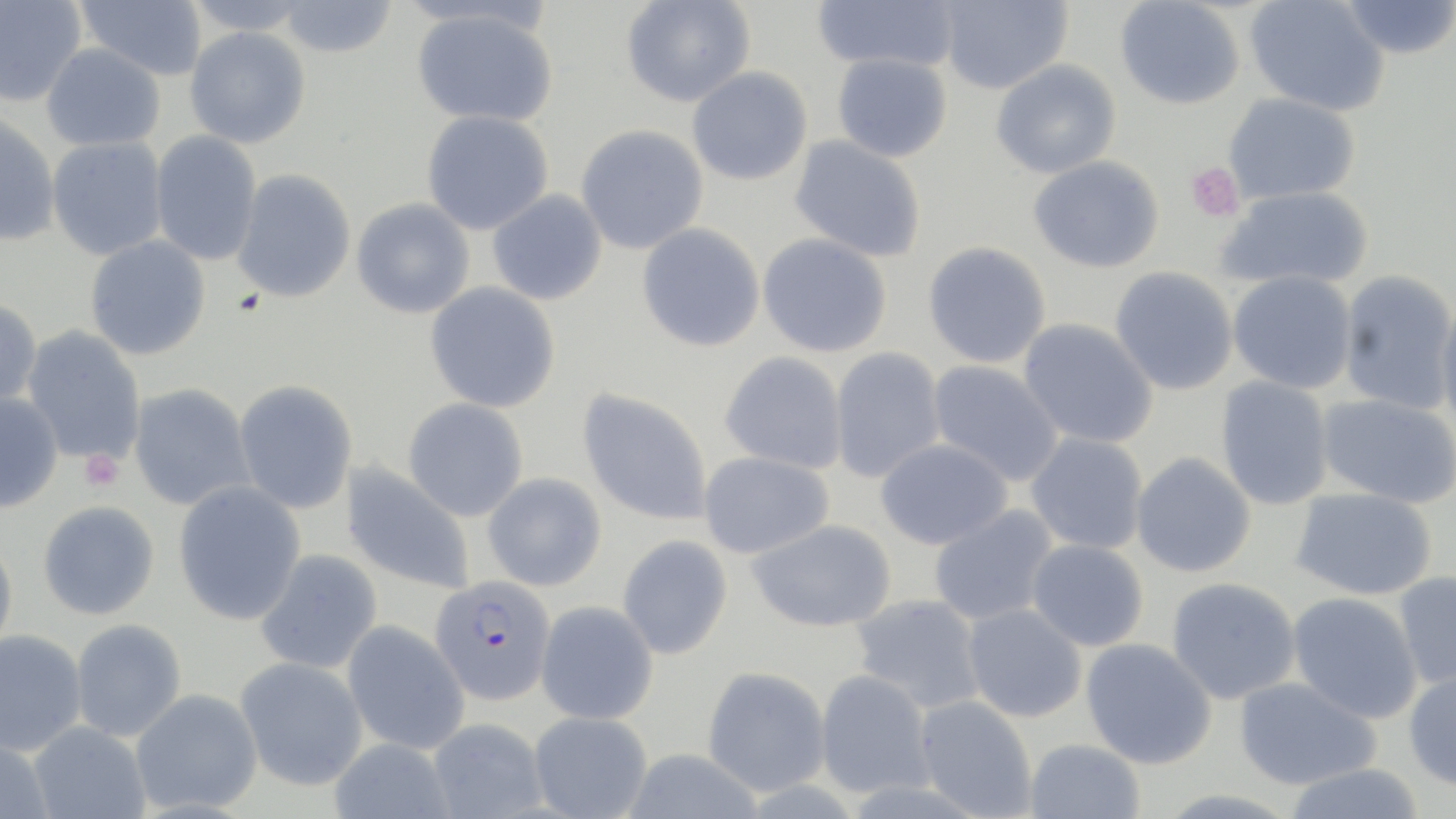 Approximate bounding boxes as named x1/y1/x2/y2 corners in pixels. Plasmodium falciparum-infected red blood cell locations: (x1=430, y1=575, x2=556, y2=705). Platelet locations: (x1=1184, y1=162, x2=1244, y2=222), (x1=79, y1=450, x2=125, y2=493). Uninfected red blood cell locations: (x1=75, y1=0, x2=208, y2=81), (x1=182, y1=0, x2=316, y2=36), (x1=276, y1=0, x2=398, y2=58), (x1=620, y1=0, x2=756, y2=108), (x1=810, y1=0, x2=960, y2=72), (x1=936, y1=0, x2=1072, y2=94), (x1=1245, y1=0, x2=1390, y2=116), (x1=1336, y1=0, x2=1456, y2=61), (x1=0, y1=1, x2=87, y2=107), (x1=1115, y1=1, x2=1245, y2=110), (x1=410, y1=7, x2=558, y2=128), (x1=184, y1=27, x2=311, y2=148), (x1=41, y1=42, x2=166, y2=152), (x1=832, y1=53, x2=952, y2=163), (x1=991, y1=59, x2=1122, y2=179), (x1=687, y1=67, x2=813, y2=186), (x1=1223, y1=93, x2=1361, y2=204), (x1=421, y1=110, x2=554, y2=235), (x1=0, y1=112, x2=61, y2=247), (x1=576, y1=125, x2=709, y2=255), (x1=149, y1=130, x2=262, y2=266), (x1=789, y1=135, x2=927, y2=262), (x1=46, y1=136, x2=168, y2=261), (x1=1028, y1=156, x2=1164, y2=274), (x1=232, y1=168, x2=356, y2=303), (x1=1217, y1=186, x2=1373, y2=292), (x1=488, y1=190, x2=607, y2=305), (x1=351, y1=198, x2=475, y2=318), (x1=637, y1=223, x2=766, y2=352), (x1=757, y1=233, x2=893, y2=358), (x1=84, y1=235, x2=211, y2=360), (x1=922, y1=242, x2=1052, y2=369), (x1=1110, y1=267, x2=1239, y2=396), (x1=1337, y1=270, x2=1456, y2=414), (x1=1227, y1=271, x2=1357, y2=394), (x1=425, y1=282, x2=561, y2=413), (x1=0, y1=297, x2=42, y2=410), (x1=1435, y1=297, x2=1456, y2=434), (x1=1018, y1=318, x2=1158, y2=449), (x1=21, y1=326, x2=146, y2=466), (x1=830, y1=347, x2=946, y2=483), (x1=720, y1=351, x2=848, y2=474), (x1=927, y1=359, x2=1064, y2=488), (x1=1215, y1=376, x2=1334, y2=510), (x1=233, y1=380, x2=358, y2=514), (x1=129, y1=383, x2=254, y2=511), (x1=577, y1=388, x2=714, y2=526), (x1=0, y1=392, x2=63, y2=513), (x1=1315, y1=393, x2=1455, y2=508), (x1=403, y1=398, x2=528, y2=521), (x1=1026, y1=433, x2=1148, y2=555), (x1=875, y1=438, x2=1012, y2=550), (x1=698, y1=451, x2=835, y2=558), (x1=1131, y1=452, x2=1256, y2=577), (x1=340, y1=462, x2=476, y2=594), (x1=483, y1=472, x2=607, y2=591), (x1=173, y1=481, x2=306, y2=625), (x1=1290, y1=488, x2=1438, y2=601), (x1=37, y1=500, x2=160, y2=620), (x1=928, y1=505, x2=1059, y2=626), (x1=747, y1=518, x2=897, y2=633), (x1=617, y1=534, x2=733, y2=660), (x1=0, y1=536, x2=18, y2=654), (x1=1026, y1=539, x2=1149, y2=652), (x1=255, y1=549, x2=382, y2=674), (x1=1392, y1=571, x2=1456, y2=692), (x1=1167, y1=577, x2=1301, y2=704), (x1=1287, y1=592, x2=1422, y2=723), (x1=850, y1=593, x2=986, y2=714), (x1=535, y1=600, x2=658, y2=724), (x1=962, y1=603, x2=1088, y2=722), (x1=70, y1=619, x2=186, y2=742), (x1=341, y1=620, x2=469, y2=755), (x1=0, y1=629, x2=86, y2=756), (x1=1081, y1=638, x2=1217, y2=769), (x1=235, y1=656, x2=367, y2=791), (x1=701, y1=665, x2=832, y2=797), (x1=1403, y1=668, x2=1456, y2=791), (x1=814, y1=669, x2=935, y2=799), (x1=1234, y1=677, x2=1381, y2=790), (x1=130, y1=688, x2=262, y2=814), (x1=914, y1=695, x2=1037, y2=817), (x1=528, y1=711, x2=653, y2=819), (x1=427, y1=717, x2=548, y2=818), (x1=27, y1=721, x2=151, y2=819), (x1=0, y1=736, x2=54, y2=819), (x1=329, y1=738, x2=455, y2=819), (x1=1024, y1=739, x2=1146, y2=819), (x1=621, y1=748, x2=765, y2=819), (x1=1282, y1=763, x2=1427, y2=819). Slide-level diagnosis: Plasmodium falciparum. May-Grünwald-Giemsa stain. Image is 1456×819 pixels. Thin blood smear. Light microscopy. One field of a larger specimen. Captured at 1000x magnification.